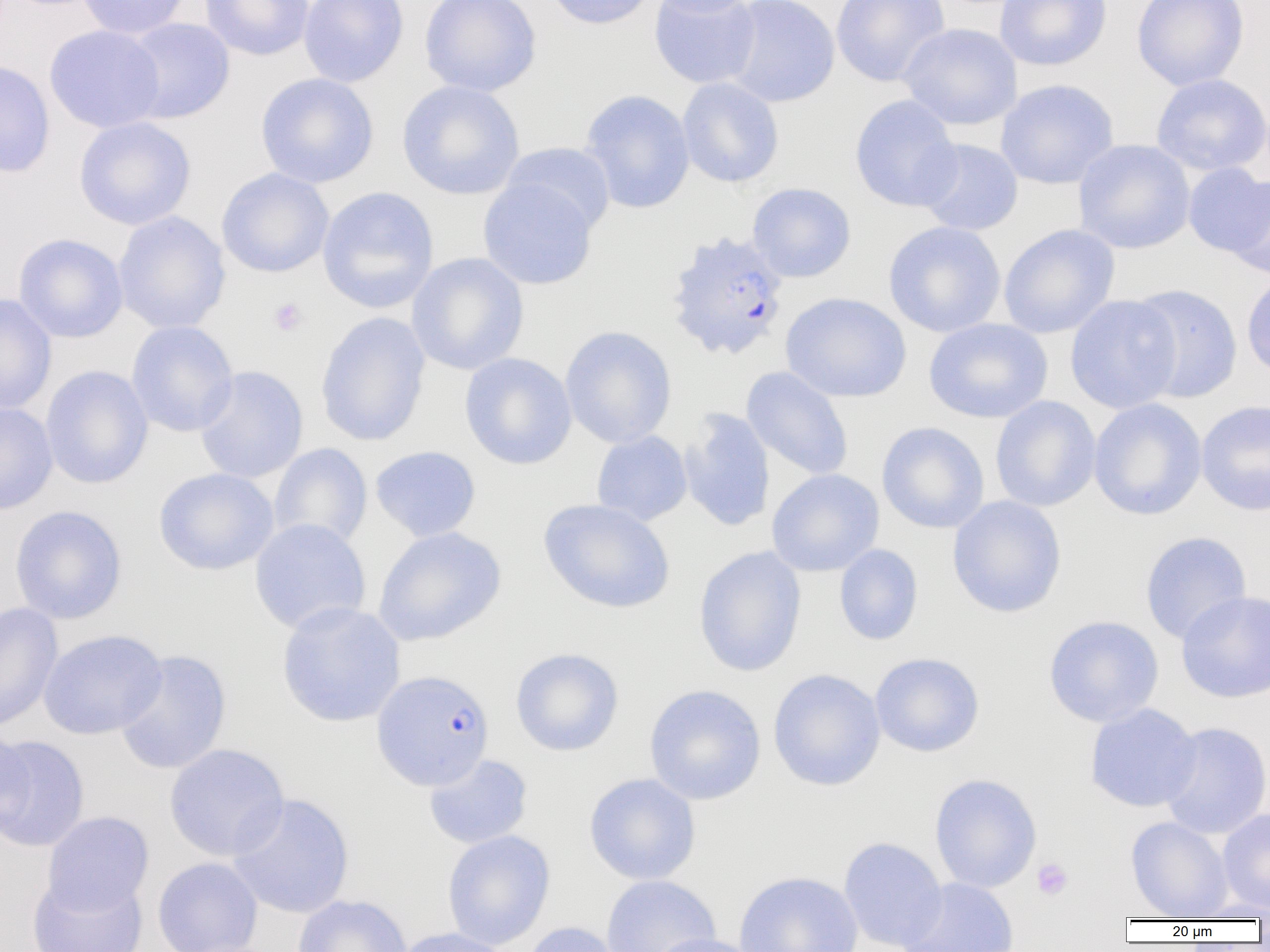
Summary:
  - Coordinate format: approximate bounding boxes as (x1, y1, x2, y2) in pixels
  - Platelet locations: (268, 297, 309, 337), (1032, 858, 1073, 900)
  - Plasmodium falciparum-infected red blood cell locations: (663, 231, 790, 362), (372, 669, 494, 790)
  - Uninfected red blood cell locations: (76, 0, 190, 40), (199, 0, 315, 61), (299, 0, 409, 87), (419, 0, 542, 97), (544, 0, 656, 30), (646, 0, 761, 16), (648, 0, 762, 89), (722, 0, 841, 107), (831, 0, 951, 87), (994, 0, 1113, 71), (1131, 0, 1250, 91), (120, 17, 236, 124), (897, 23, 1022, 130), (44, 24, 166, 133), (0, 60, 56, 179), (255, 73, 379, 189), (1151, 73, 1270, 176), (677, 77, 784, 188), (995, 79, 1119, 189), (396, 80, 525, 200), (578, 89, 695, 214), (849, 94, 962, 212), (73, 116, 196, 230), (915, 138, 1023, 235), (1073, 139, 1195, 254), (501, 142, 616, 235), (1182, 164, 1269, 256), (216, 168, 335, 278), (1226, 175, 1270, 280), (478, 177, 598, 290), (746, 182, 857, 283), (317, 186, 439, 314), (112, 211, 231, 334), (883, 221, 1006, 337), (998, 223, 1120, 339), (13, 233, 129, 343), (406, 252, 529, 375), (1241, 270, 1270, 380), (1127, 283, 1244, 404), (780, 292, 913, 403), (0, 293, 57, 416), (1065, 294, 1183, 414), (315, 311, 431, 447), (923, 318, 1053, 424), (126, 320, 239, 437), (559, 325, 677, 448), (459, 352, 577, 470), (40, 365, 154, 489), (194, 365, 309, 484), (741, 366, 854, 481), (990, 395, 1101, 512), (1088, 398, 1208, 521), (1196, 400, 1270, 516), (0, 401, 58, 514), (678, 407, 776, 532), (876, 421, 990, 534), (591, 431, 692, 526), (269, 443, 372, 551), (369, 446, 481, 542), (153, 467, 279, 576), (766, 469, 884, 576), (947, 495, 1067, 618), (538, 498, 675, 614), (9, 505, 128, 624), (249, 518, 371, 634), (373, 527, 506, 646), (1139, 531, 1252, 645), (834, 544, 923, 646), (693, 545, 807, 677), (1176, 590, 1270, 704), (276, 601, 406, 727), (0, 603, 63, 733), (1043, 615, 1164, 727), (38, 629, 167, 740), (510, 647, 624, 756), (113, 649, 232, 774), (869, 652, 985, 757), (767, 668, 886, 791), (644, 684, 766, 805), (1084, 703, 1202, 812), (1158, 721, 1270, 839), (1, 730, 34, 842), (0, 733, 90, 852), (164, 743, 289, 862), (423, 753, 533, 849), (929, 772, 1042, 893), (583, 773, 701, 885), (228, 793, 355, 919), (1217, 808, 1270, 913), (42, 811, 154, 914), (1125, 816, 1232, 919), (441, 829, 556, 950), (838, 836, 948, 951), (152, 857, 263, 952), (732, 870, 865, 952), (27, 872, 148, 952), (601, 875, 721, 952), (899, 877, 1020, 952), (292, 894, 412, 952), (1187, 901, 1270, 921), (520, 921, 625, 952), (392, 927, 516, 952), (646, 933, 762, 952)
  - Slide-level diagnosis: Plasmodium falciparum
  - Preparation: thin blood smear
  - Field of view: single
  - Modality: optical microscopy
  - Magnification: 1000x
  - Image size: 1270×952 pixels